Assess this cell for malaria.
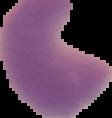
Parasitized.

Image is 112×118 pixels. From a thin blood smear. Cell region segmented out of the field of view; the surrounding area is masked to black.